Comment on the morphology of the erythrocytes.
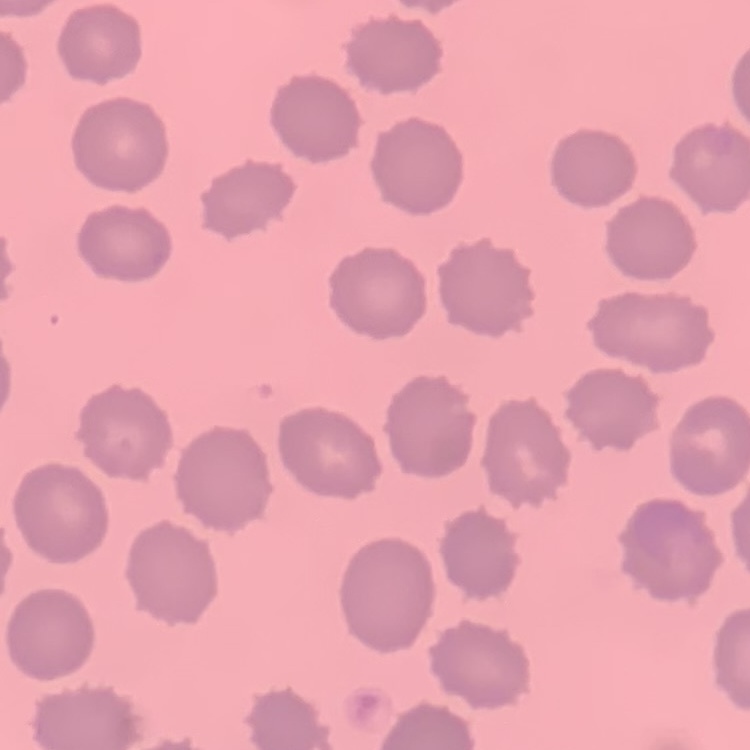

No rouleaux formation.

{
  "image_type": "one tile cut from a larger photomicrograph",
  "stain": "Field's or Giemsa",
  "preparation": "thin blood smear"
}